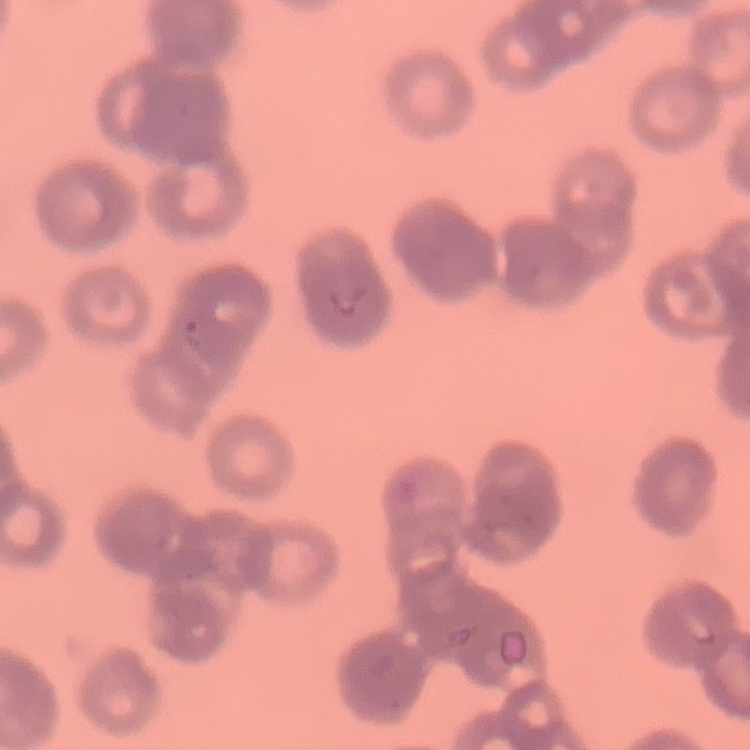
Summary:
  - Erythrocyte morphology: rouleaux formation
  - Preparation: thin blood smear
  - Image type: square crop of a larger photomicrograph
  - Stain: Field's or Giemsa